Name the blood parasite species.
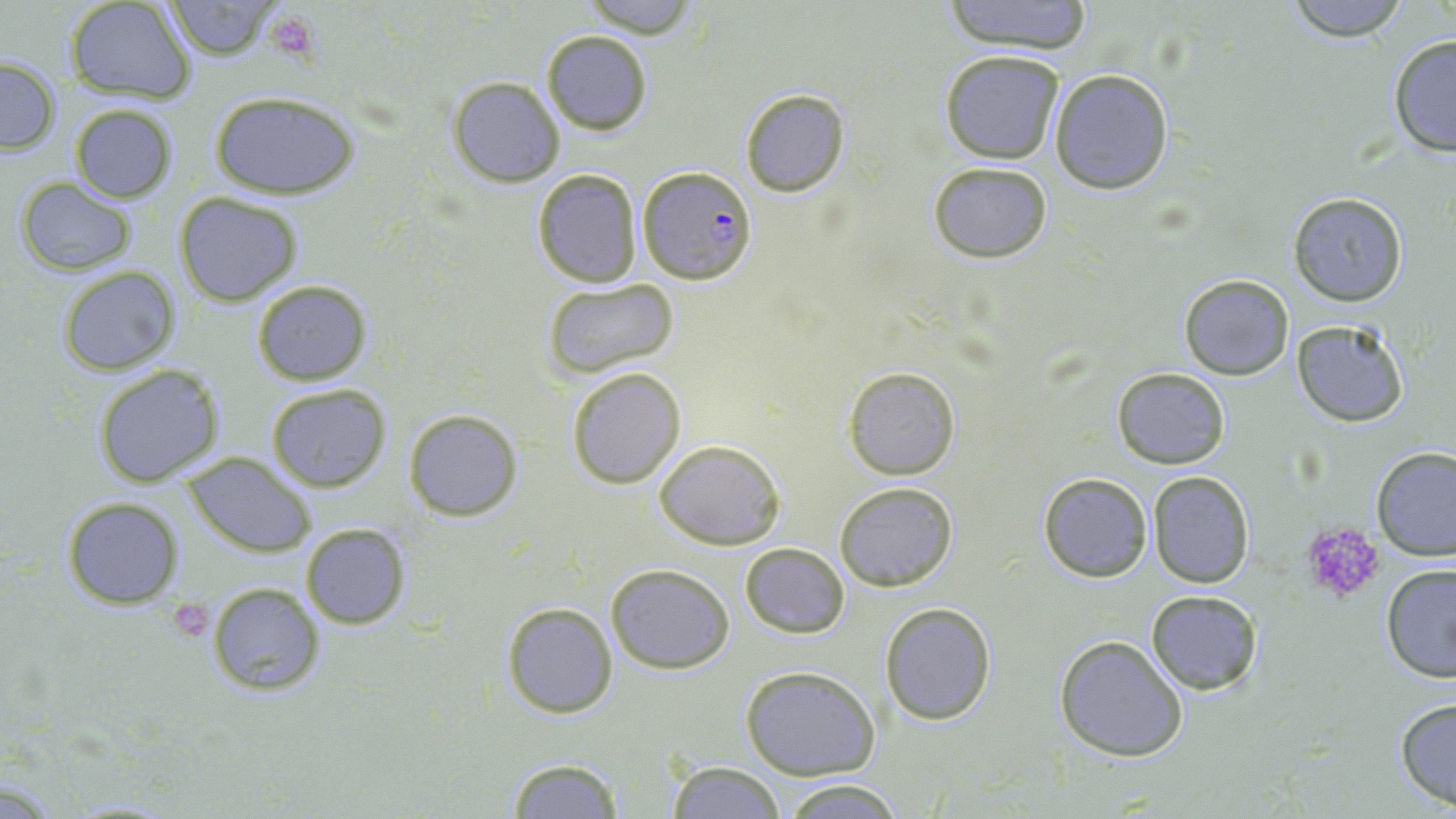

Plasmodium falciparum.

Approximate bounding boxes as (x1, y1, x2, y2) in pixels. Uninfected red blood cell locations: (65, 0, 195, 102), (163, 0, 285, 59), (577, 0, 700, 40), (940, 0, 1094, 52), (1279, 0, 1415, 42), (540, 30, 653, 135), (1386, 33, 1456, 160), (941, 50, 1065, 164), (0, 56, 61, 156), (1049, 68, 1175, 194), (447, 76, 565, 187), (739, 89, 849, 197), (209, 91, 361, 200), (68, 104, 179, 202), (930, 162, 1053, 261), (531, 167, 644, 288), (12, 176, 141, 276), (173, 191, 305, 306), (1288, 192, 1408, 307), (57, 266, 182, 377), (1179, 274, 1292, 380), (541, 277, 679, 380), (250, 279, 373, 387), (1293, 318, 1411, 427), (92, 363, 227, 488), (566, 366, 686, 488), (844, 366, 961, 479), (1112, 366, 1229, 469), (265, 384, 392, 493), (403, 408, 523, 521), (654, 438, 784, 550), (1368, 447, 1456, 561), (181, 453, 316, 555), (1148, 470, 1253, 588), (1038, 472, 1152, 583), (834, 481, 958, 592), (61, 496, 184, 608), (300, 522, 410, 629), (739, 542, 849, 639), (1380, 563, 1456, 684), (607, 564, 733, 674), (206, 581, 325, 698), (1145, 589, 1264, 696), (500, 602, 618, 718), (880, 602, 998, 725), (1054, 634, 1189, 761), (739, 665, 881, 781), (1394, 696, 1456, 812), (505, 757, 626, 818), (667, 763, 785, 818), (777, 778, 911, 817). Plasmodium falciparum-infected red blood cell locations: (638, 165, 757, 284). Platelet locations: (262, 10, 321, 65), (1301, 522, 1386, 603), (174, 604, 212, 640). Captured at 1000x magnification. Image is 1456×819 pixels. Optical microscopy. Thin blood film. May-Grünwald-Giemsa-stained preparation. One field of a larger specimen.